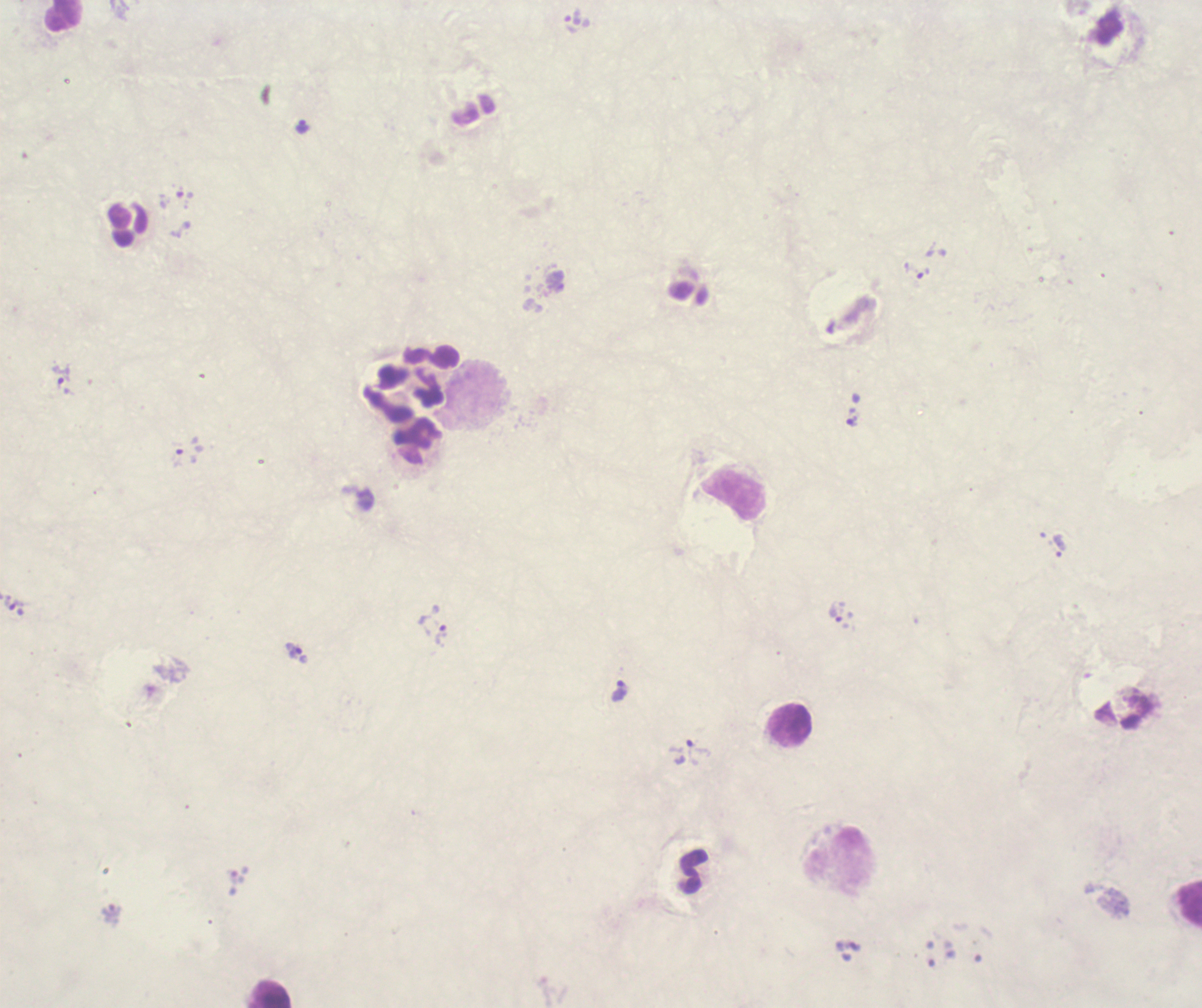
Approximate centers as [x, y] in pixels.
Summary:
  - Trophozoite locations: [572, 17], [302, 128], [916, 271], [61, 375], [852, 421], [189, 450], [1059, 546], [12, 603], [835, 614], [441, 635], [294, 651], [620, 690], [692, 753]
  - Leukocyte locations: [65, 16], [476, 391], [405, 394], [790, 725], [1190, 904], [271, 994]
  - Magnification: 100x
  - Coloration quality: bad
  - Background quality: unsatisfactory
  - Context: previously used in a real diagnosis
  - Image size: 1202×1008 pixels
  - Result: positive for Plasmodium parasites
  - Field of view: single
  - Stain: Romanowsky
  - Preparation: thick smear of blood